Report the malaria status of this cell.
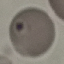
It is parasitized.

Summary:
  - Capture: smartphone through the microscope eyepiece
  - Image type: automatically extracted cell patch, resized to 64 × 64 pixels
  - Stain: Giemsa
  - Preparation: thin blood film